Classify this cell by malaria status.
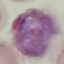

It is parasitized.

Automatically extracted cell patch, resized to 64 × 64 pixels. Thin blood smear. Giemsa stain. Acquired by smartphone through the microscope eyepiece.